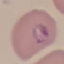

malaria status = parasitized
capture = smartphone through the microscope eyepiece
stain = Giemsa
image type = automatically extracted cell patch, resized to 64 × 64 pixels
preparation = thin smear